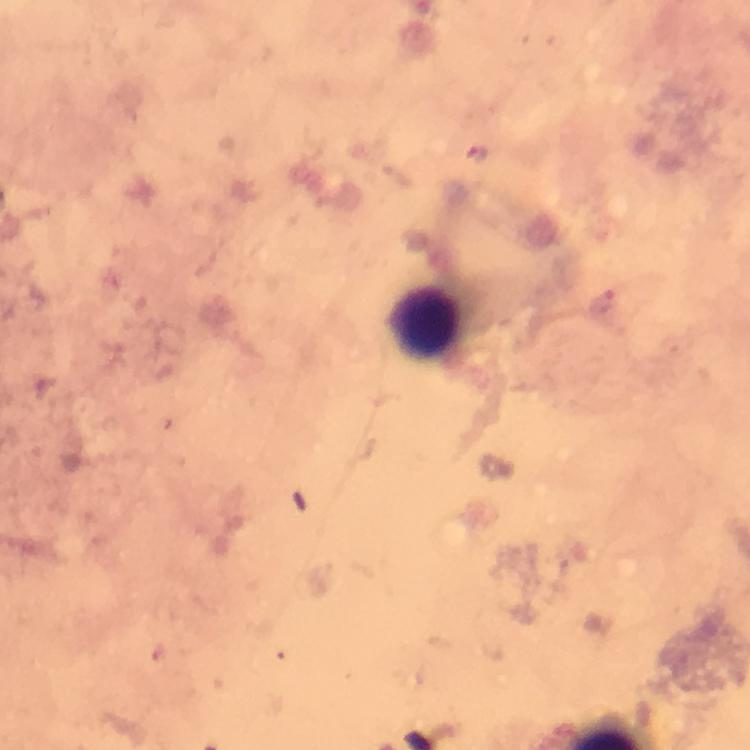
cropped from = one field of view
preparation = thick smear
Plasmodium parasites = none detected
immersion oil = used
stain = Giemsa
context = from a malaria diagnostic workup
capture = smartphone camera through the microscope
image size = 750×750 pixels
magnification = 100x
leukocyte locations = approximate centers as {x, y} in pixels: {427, 324}